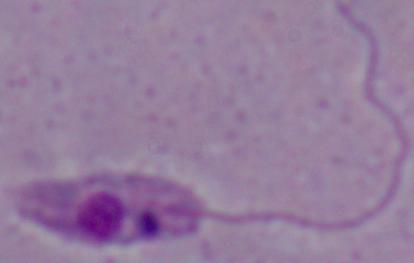
Photomicrograph. 1000x magnification. A Leishmania parasite is seen.